Name the blood parasite species.
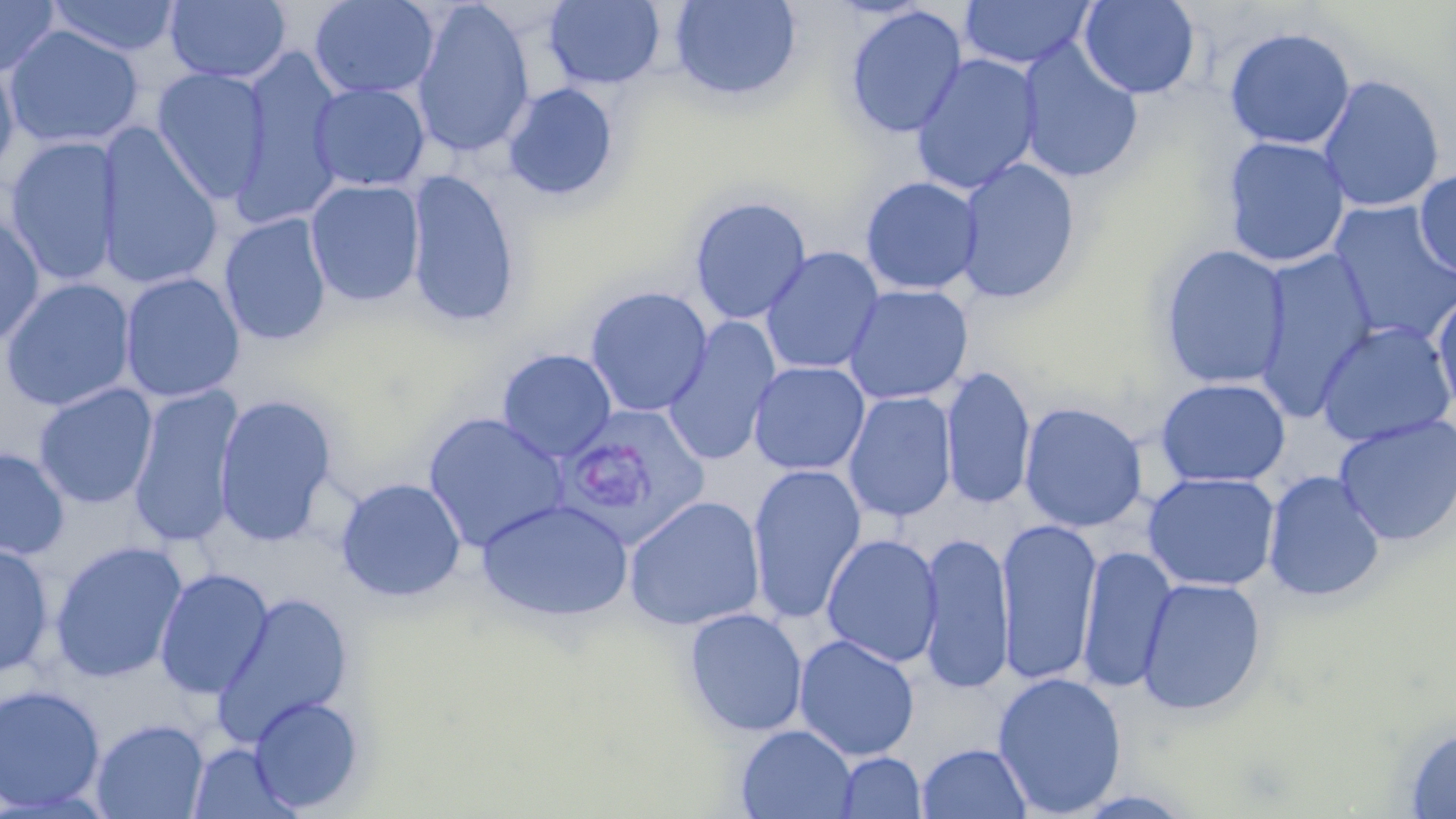

Plasmodium vivax.

Approximate bounding boxes as [x1, y1, x2, y2] in pixels. Uninfected red blood cell locations: [0, 0, 61, 78], [43, 0, 183, 58], [309, 0, 440, 100], [545, 0, 666, 90], [669, 0, 802, 102], [959, 0, 1095, 70], [1078, 0, 1200, 99], [164, 1, 291, 85], [411, 2, 535, 161], [844, 5, 968, 139], [3, 24, 144, 150], [1223, 26, 1356, 151], [1015, 39, 1144, 185], [230, 47, 348, 230], [0, 52, 20, 182], [910, 52, 1043, 195], [151, 67, 271, 203], [1316, 73, 1446, 213], [310, 82, 430, 191], [503, 83, 619, 202], [95, 123, 224, 293], [2, 136, 122, 287], [1222, 136, 1350, 269], [955, 157, 1081, 305], [404, 168, 522, 330], [1413, 168, 1456, 280], [860, 175, 983, 296], [305, 179, 425, 307], [688, 195, 811, 325], [1327, 201, 1456, 345], [0, 210, 45, 351], [218, 212, 333, 347], [1158, 244, 1290, 389], [760, 246, 885, 375], [1252, 249, 1379, 421], [119, 271, 245, 403], [0, 278, 136, 412], [842, 284, 974, 405], [584, 286, 713, 417], [1432, 289, 1456, 420], [662, 316, 781, 467], [1315, 321, 1456, 448], [497, 349, 617, 461], [747, 361, 870, 476], [941, 364, 1035, 510], [1155, 377, 1290, 488], [33, 383, 157, 509], [127, 385, 244, 549], [842, 391, 957, 524], [213, 392, 339, 547], [1019, 401, 1148, 532], [422, 412, 568, 553], [1333, 414, 1456, 546], [0, 447, 70, 561], [746, 464, 867, 624], [1263, 470, 1386, 602], [1143, 471, 1281, 592], [335, 477, 466, 602], [624, 495, 766, 631], [476, 499, 633, 622], [996, 517, 1101, 688], [918, 531, 1016, 696], [821, 533, 942, 668], [50, 540, 188, 683], [0, 542, 54, 678], [1077, 545, 1177, 693], [154, 568, 273, 699], [1137, 576, 1267, 716], [212, 591, 355, 747], [683, 607, 808, 737], [794, 634, 920, 761], [992, 671, 1126, 817], [0, 684, 106, 813], [247, 695, 366, 813], [90, 718, 209, 819], [735, 724, 857, 819], [1404, 726, 1456, 817], [188, 742, 301, 819], [917, 743, 1032, 819], [834, 751, 928, 818]. Plasmodium vivax-infected red blood cell locations: [557, 405, 710, 547]. Thin blood smear. Captured at 1000x magnification. Image is 1456×819 pixels. One field of a larger specimen. May-Grünwald-Giemsa-stained preparation. Light microscopy.